Locate every uninfected red blood cell.
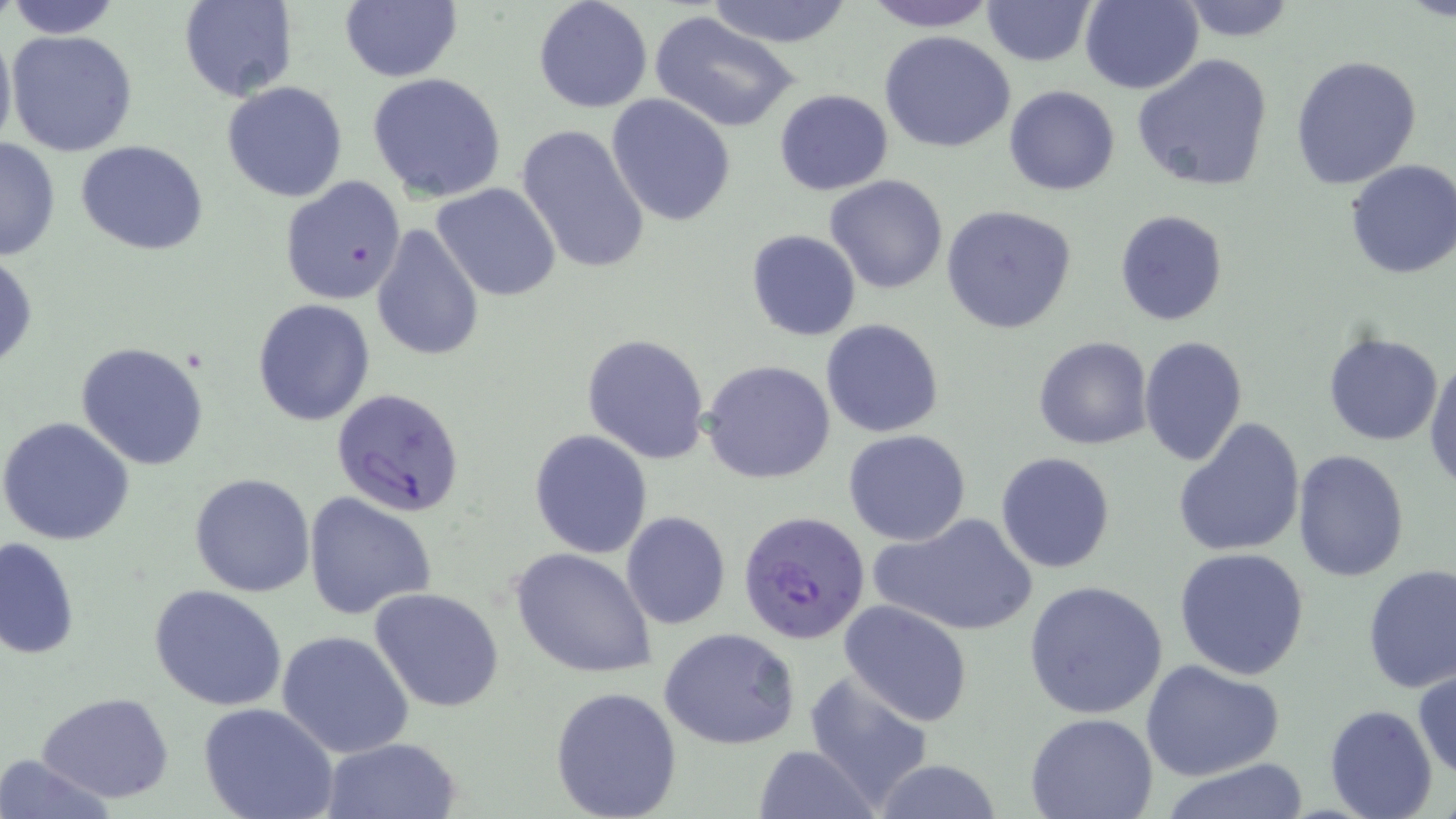
Approximate bounding boxes as [x1, y1, x2, y2] in pixels.
Uninfected red blood cells: [5, 0, 125, 38], [339, 0, 462, 83], [532, 0, 653, 113], [704, 0, 854, 46], [860, 0, 1001, 31], [981, 0, 1097, 67], [1177, 0, 1300, 42], [177, 1, 297, 101], [1079, 1, 1203, 94], [650, 10, 802, 132], [0, 24, 16, 160], [6, 29, 139, 158], [880, 31, 1017, 153], [1131, 53, 1278, 195], [1290, 55, 1423, 190], [367, 72, 508, 202], [221, 81, 349, 202], [1004, 86, 1120, 196], [773, 88, 893, 196], [606, 94, 735, 227], [516, 124, 652, 274], [0, 135, 61, 263], [76, 140, 209, 254], [1343, 160, 1456, 280], [825, 174, 948, 294], [279, 175, 407, 305], [432, 183, 562, 301], [941, 205, 1076, 334], [1115, 209, 1229, 328], [370, 224, 485, 362], [746, 229, 861, 341], [1, 252, 38, 372], [252, 298, 376, 427], [821, 318, 945, 439], [1323, 330, 1443, 446], [581, 333, 710, 464], [1138, 334, 1249, 468], [1033, 336, 1152, 451], [75, 340, 211, 470], [1425, 353, 1456, 490], [702, 360, 837, 485], [1, 416, 135, 546], [1173, 418, 1306, 559], [529, 429, 653, 558], [843, 429, 972, 546], [1293, 449, 1410, 580], [994, 451, 1116, 575], [188, 472, 316, 597], [302, 490, 438, 621], [620, 510, 731, 631], [870, 511, 1039, 637], [0, 536, 79, 661], [511, 547, 657, 678], [1173, 548, 1311, 680], [1361, 564, 1456, 694], [1023, 580, 1169, 719], [148, 584, 288, 711], [370, 588, 505, 713], [838, 598, 975, 726], [661, 628, 803, 749], [276, 630, 416, 759], [1141, 660, 1284, 783], [1413, 666, 1456, 782], [805, 671, 935, 808], [548, 685, 683, 819], [37, 693, 176, 805], [199, 703, 338, 819], [1324, 705, 1438, 819], [1025, 713, 1158, 819], [319, 736, 463, 818], [754, 745, 877, 819], [1, 753, 116, 819], [869, 759, 1007, 818], [1156, 760, 1313, 819].

slide-level diagnosis = Plasmodium falciparum
stain = May-Grünwald-Giemsa
field of view = single
image size = 1456×819 pixels
magnification = 1000x
Plasmodium falciparum-infected red blood cell locations = approximate bounding boxes as [x1, y1, x2, y2] in pixels: [332, 388, 465, 518], [738, 511, 871, 644]
modality = light microscopy
preparation = thin blood smear